Locate every malaria parasite and every leukocyte.
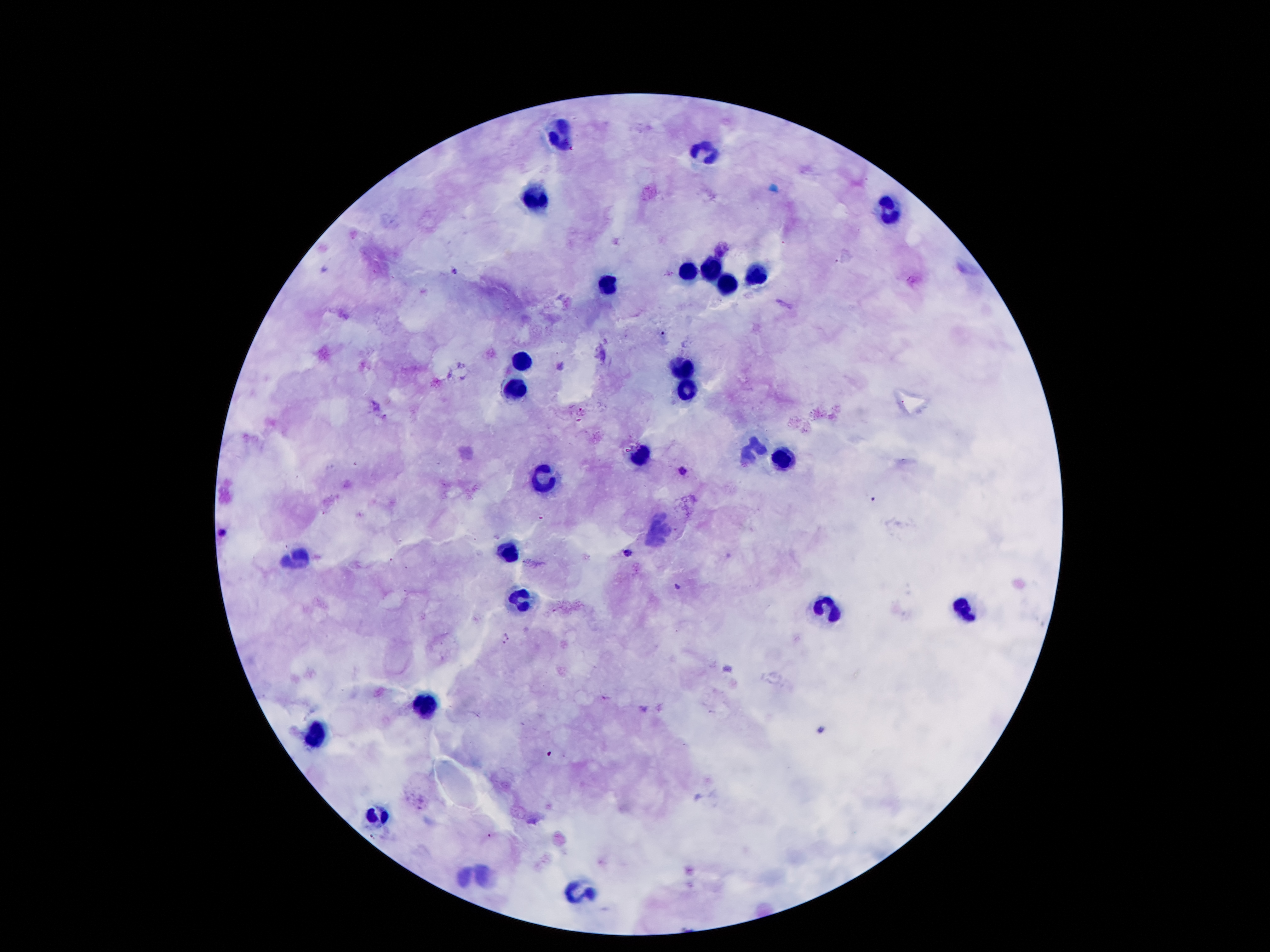
Approximate object centers, in pixels from the top-left corner.
Malaria parasites: (x=455, y=271), (x=581, y=410), (x=682, y=471), (x=873, y=499), (x=224, y=533), (x=628, y=552), (x=677, y=586), (x=506, y=639), (x=605, y=697).
Leukocytes: (x=564, y=135), (x=701, y=153), (x=537, y=200), (x=892, y=208), (x=685, y=270), (x=710, y=270), (x=757, y=271), (x=607, y=286), (x=728, y=286), (x=522, y=359), (x=683, y=368), (x=516, y=384), (x=690, y=385), (x=752, y=447), (x=639, y=455), (x=782, y=459), (x=540, y=476), (x=659, y=532), (x=509, y=554), (x=301, y=555), (x=521, y=598), (x=964, y=608), (x=826, y=612), (x=425, y=707), (x=316, y=740), (x=380, y=813), (x=460, y=876), (x=487, y=880), (x=577, y=891).

Summary:
  - Magnification: 100x
  - Preparation: thick blood film
  - Image size: 1270×952 pixels
  - Stain: Giemsa
  - Patient malaria status: infected with Plasmodium falciparum
  - Field of view: single
  - Capture: smartphone through the microscope eyepiece